Assess the morphology of the erythrocytes.
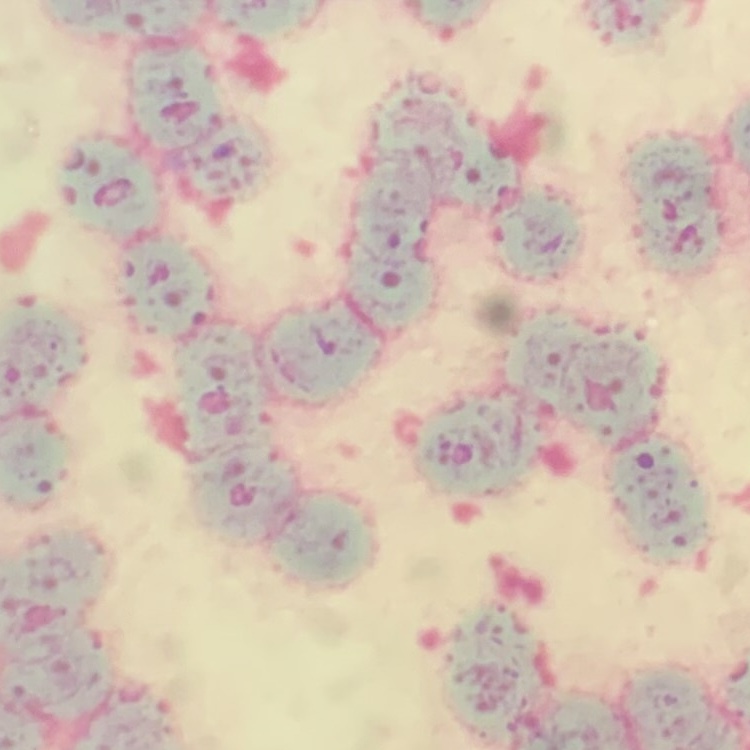

Rouleaux formation.

stain: Field's or Giemsa
image_type: square crop of a larger photomicrograph
preparation: thin peripheral smear